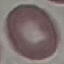
Summary:
  - Malaria status: uninfected
  - Capture: smartphone through the microscope eyepiece
  - Image type: automatically extracted cell patch, resized to 64 × 64 pixels
  - Stain: Giemsa
  - Preparation: thin blood smear